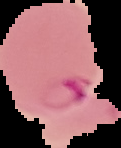
image type = segmented cell region with the area outside set to black
image size = 121×148 pixels
result = Plasmodium parasites identified
preparation = thin blood film